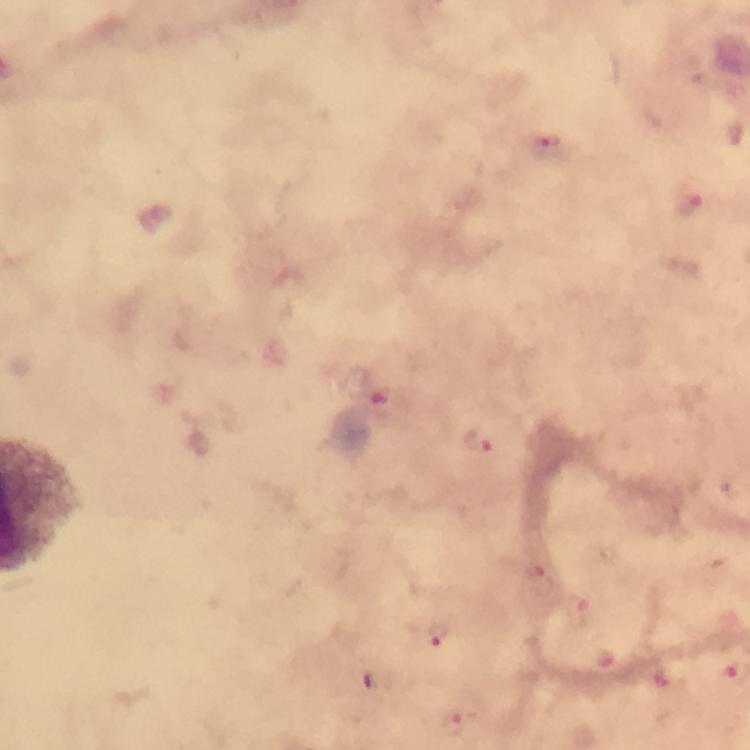
immersion oil = applied
cropped from = a single field of view
context = from a diagnostic examination for malaria
magnification = 100x
preparation = thick smear
stain = Giemsa
malaria parasite locations = approximate centers as [x, y] in pixels: [543, 151], [686, 202], [382, 395], [476, 439], [529, 569], [581, 615], [436, 633], [452, 722]
capture = smartphone photograph through a microscope
image size = 750×750 pixels